Identify the blood parasite species.
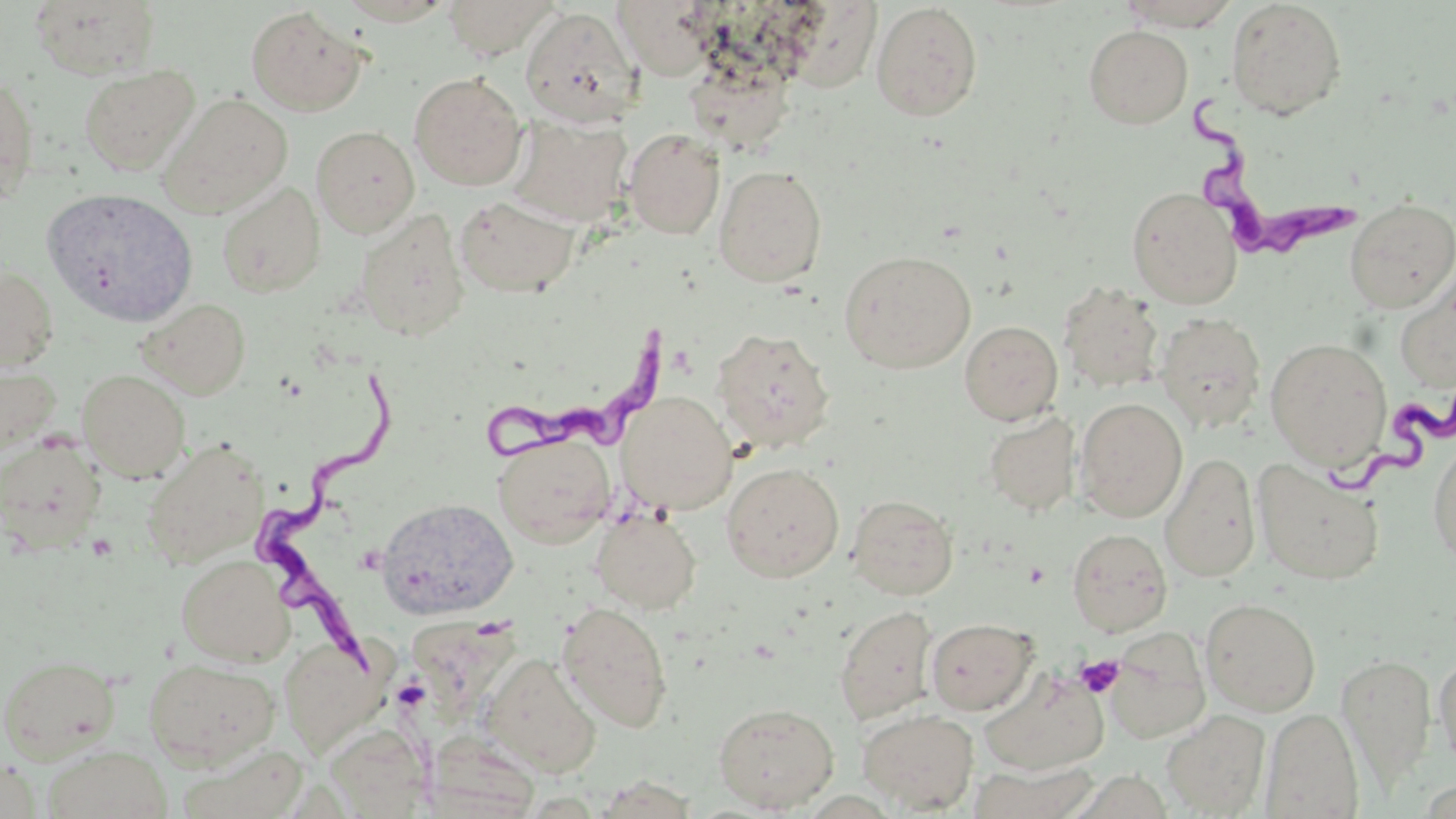
Trypanosoma brucei.

Summary:
  - Coordinate format: approximate bounding boxes as (x1,y1)-(x2,y2) corner pairs in pixels
  - Trypanosoma brucei locations: (1181,89)-(1354,262), (487,325)-(692,466), (260,371)-(412,680), (1314,389)-(1455,501)
  - Uninfected red blood cell locations: (441,0)-(559,60), (29,1)-(161,80), (614,1)-(717,81), (1225,1)-(1347,120), (870,2)-(983,122), (1113,2)-(1244,30), (245,6)-(367,116), (520,7)-(641,127), (1084,25)-(1193,128), (684,58)-(795,154), (78,64)-(200,175), (409,72)-(527,191), (0,74)-(40,206), (159,92)-(294,218), (508,114)-(633,228), (311,126)-(420,237), (624,128)-(725,239), (714,164)-(828,288), (216,180)-(326,298), (1127,186)-(1243,309), (41,187)-(200,328), (454,194)-(581,299), (1343,198)-(1456,313), (354,209)-(469,342), (839,250)-(976,373), (0,266)-(59,371), (1395,275)-(1456,395), (1058,282)-(1165,394), (136,297)-(251,399), (1155,312)-(1266,432), (959,320)-(1063,425), (712,327)-(836,454), (1265,337)-(1392,469), (0,357)-(61,462), (77,369)-(190,483), (616,391)-(736,515), (1074,397)-(1188,522), (983,411)-(1081,516), (494,433)-(615,548), (0,434)-(105,549), (1428,435)-(1456,571), (141,438)-(271,569), (1160,452)-(1261,583), (1252,458)-(1386,584), (721,462)-(845,582), (846,493)-(958,600), (375,497)-(518,619), (591,509)-(701,614), (1066,527)-(1172,637), (176,554)-(295,667), (1201,597)-(1321,716), (556,601)-(674,733), (834,605)-(939,725), (925,618)-(1037,716), (1104,629)-(1211,744), (278,636)-(388,754), (1434,651)-(1456,771), (482,652)-(602,777), (0,654)-(121,762), (1337,654)-(1437,785), (143,657)-(280,768), (979,667)-(1109,775), (713,702)-(840,813), (1261,708)-(1363,818), (857,709)-(979,814), (1162,710)-(1271,817), (326,725)-(433,817), (422,732)-(541,819), (179,741)-(309,819), (42,743)-(173,819), (0,756)-(41,818), (967,761)-(1103,819)
  - Platelet locations: (1075,654)-(1123,698)
  - Magnification: 1000x
  - Image size: 1456×819 pixels
  - Stain: May-Grünwald-Giemsa
  - Modality: optical microscopy
  - Preparation: thin blood film
  - Field of view: one of a larger specimen